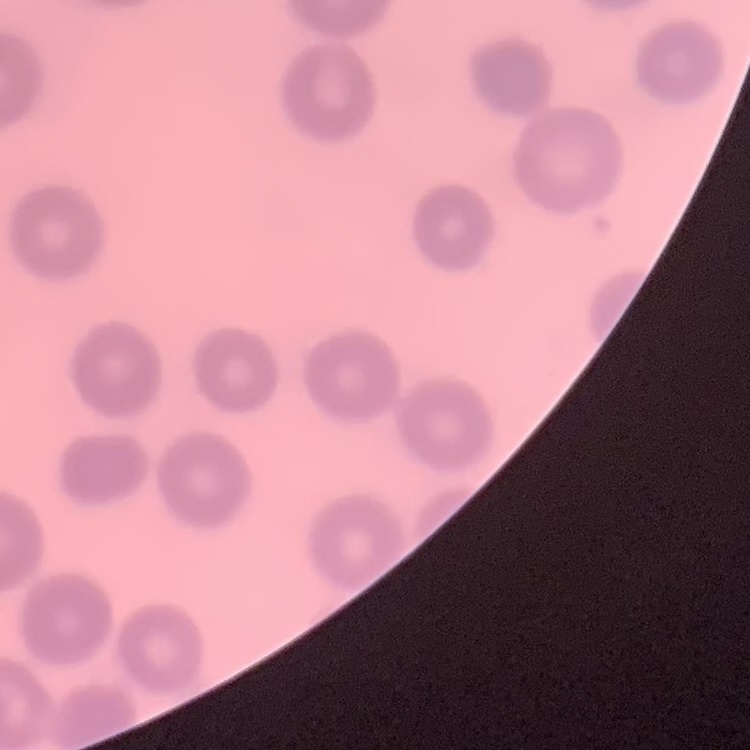
Summary:
  - Red blood cell morphology: no rouleaux formation
  - Image type: one tile cut from a larger photomicrograph
  - Stain: Field's or Giemsa
  - Preparation: thin blood film